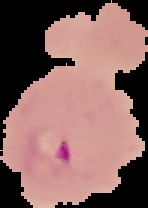
Summary:
  - Image size: 148×208 pixels
  - Image type: segmented cell region with the area outside set to black
  - Result: malaria parasites identified
  - Preparation: thin blood smear